Assess the morphology of the red blood cells.
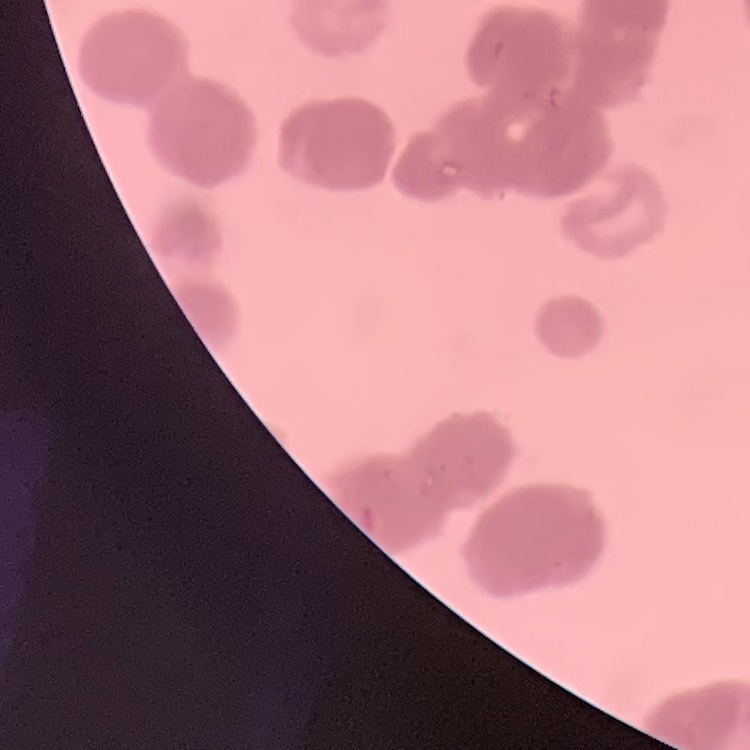

They show rouleaux formation.

Thin blood smear. Field's or Giemsa stain. Square crop of a larger photomicrograph.